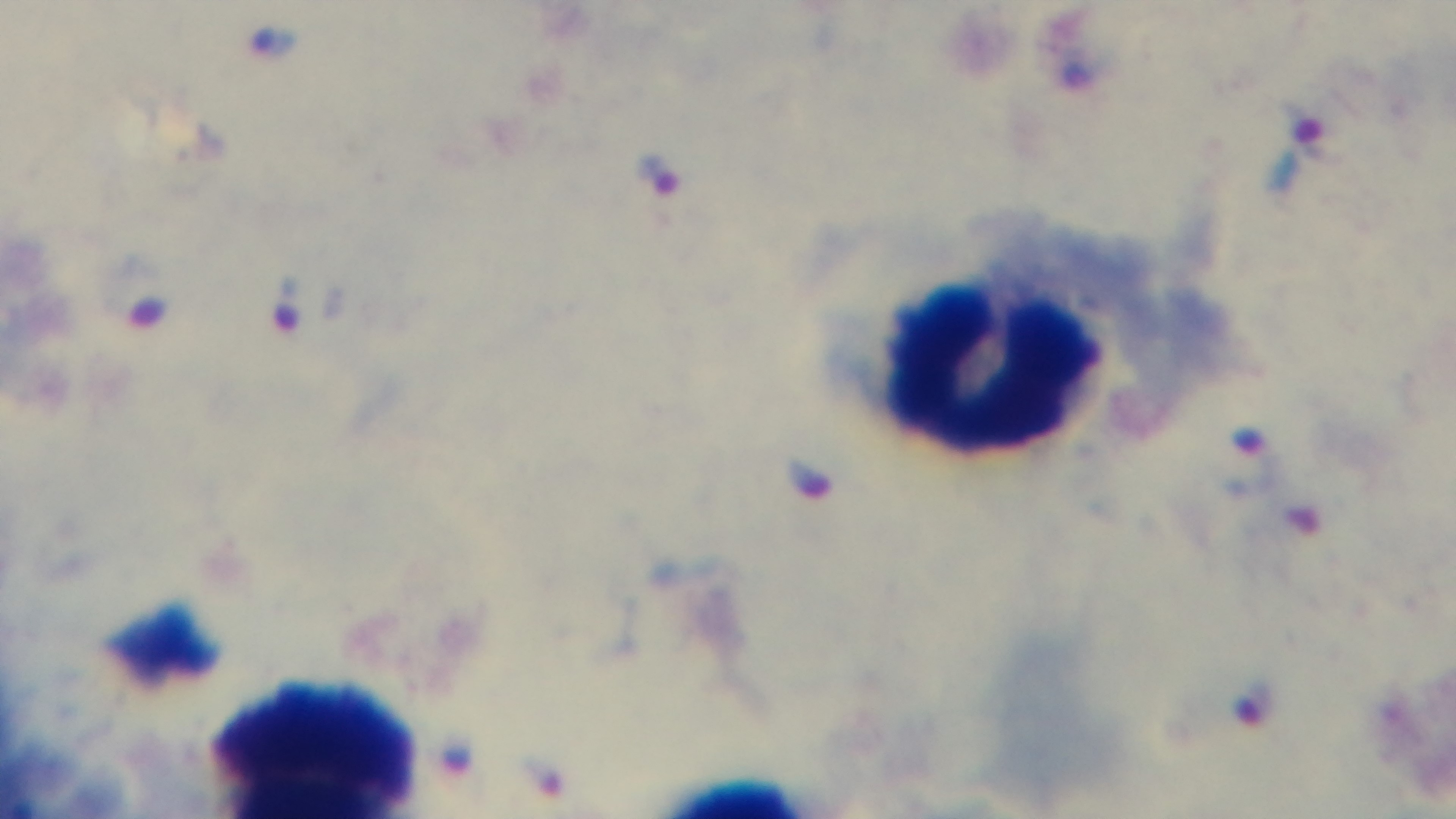

One field from the slide. Captured with a mounted 4K digital camera. Giemsa-stained. Photomicrograph. Preparation: thick. Malaria status: positive. 100x oil-immersion objective.